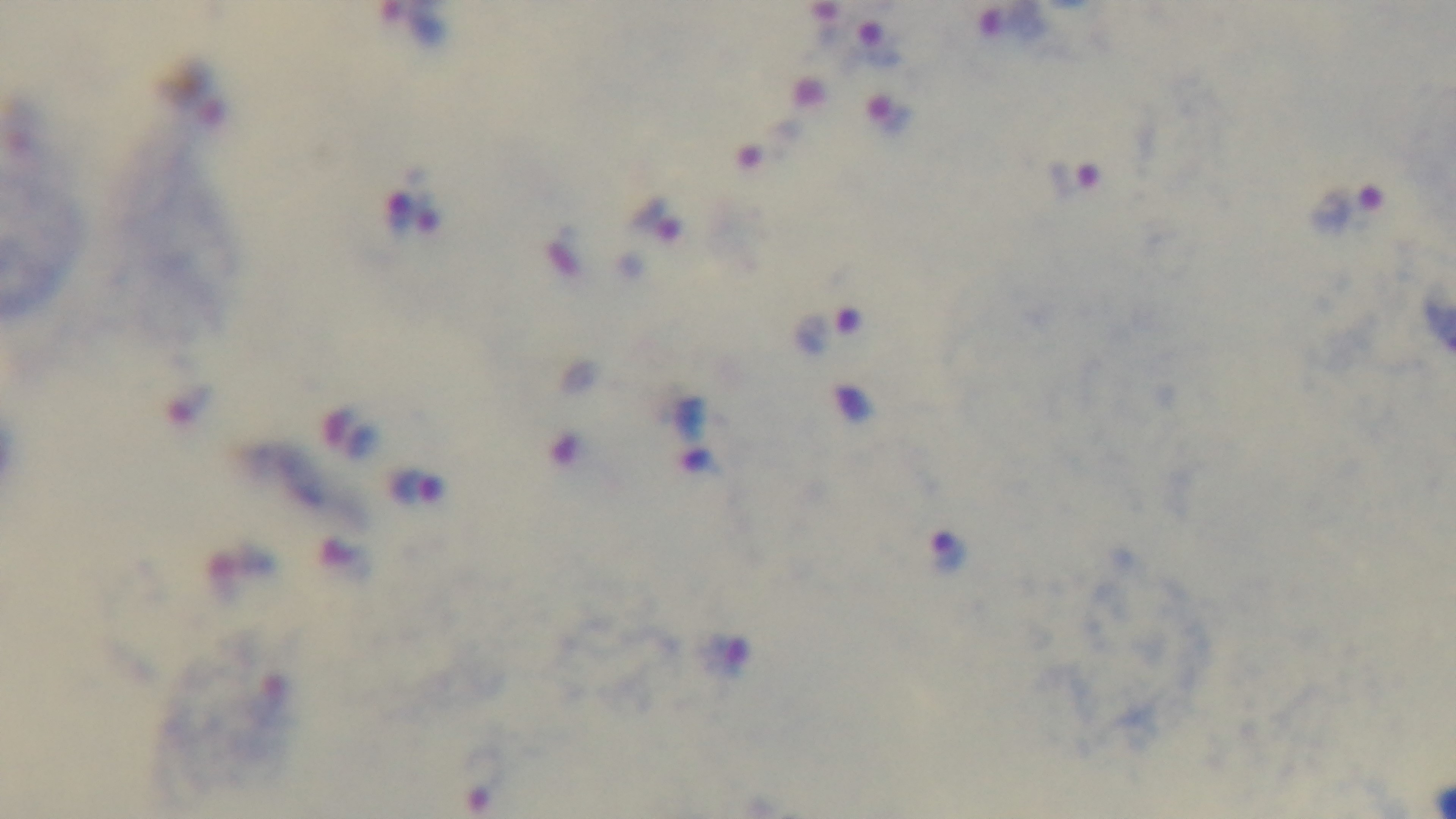

modality = light microscopy
stain = Giemsa
malaria status = positive
objective = 100x oil immersion
preparation = thick
field of view = one from the slide
capture = mounted 4K digital camera